Report the malaria status of this cell.
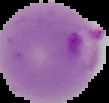
Parasitized.

preparation = thin blood film
image type = segmented cell region on a black background
image size = 109×103 pixels